State which parasite is depicted.
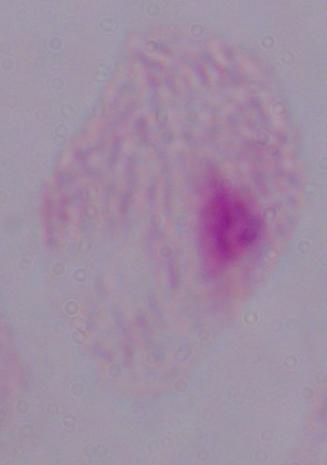
This is a trichomonad.

{
  "magnification": "1000x",
  "modality": "micrograph"
}